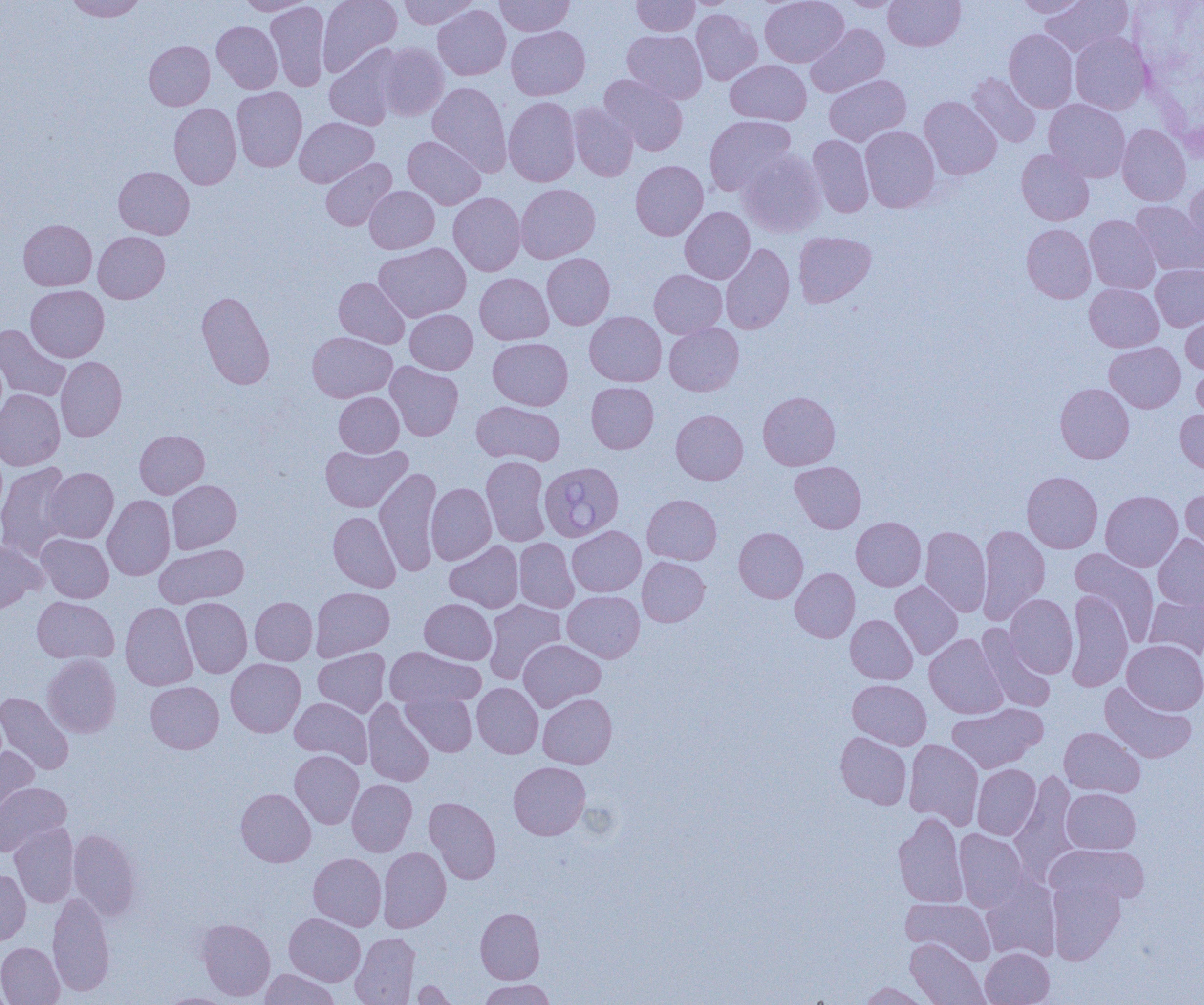
Summary:
  - Coordinate format: approximate bounding boxes as (x1,y1)-(x2,y2) corner pairs in pixels
  - Uninfected red blood cell locations: (64,0)-(147,21), (318,0)-(402,76), (399,0)-(479,29), (495,0)-(575,36), (631,0)-(699,36), (681,0)-(743,8), (760,0)-(848,67), (839,0)-(903,11), (884,0)-(965,51), (1015,0)-(1091,17), (1040,0)-(1132,57), (235,1)-(314,15), (266,2)-(330,91), (433,4)-(511,80), (691,9)-(763,84), (212,21)-(282,93), (806,24)-(889,97), (506,26)-(590,100), (1004,29)-(1078,113), (622,30)-(707,103), (1070,31)-(1151,114), (144,41)-(215,110), (378,43)-(449,121), (325,46)-(403,130), (726,60)-(811,125), (967,73)-(1041,147), (600,74)-(688,155), (824,74)-(911,145), (428,82)-(511,175), (231,87)-(307,172), (504,96)-(580,187), (920,96)-(1001,179), (1043,99)-(1130,182), (168,103)-(241,189), (568,103)-(638,181), (704,115)-(796,196), (294,117)-(378,187), (1117,123)-(1191,206), (860,126)-(940,212), (808,134)-(874,217), (403,135)-(486,209), (738,149)-(826,237), (1016,149)-(1094,225), (321,158)-(396,231), (630,160)-(708,240), (114,166)-(194,239), (1185,181)-(1204,260), (516,183)-(600,263), (364,186)-(439,253), (449,192)-(526,276), (1131,201)-(1204,276), (680,206)-(755,283), (1085,215)-(1160,294), (18,219)-(96,290), (1022,224)-(1096,303), (93,231)-(170,303), (794,232)-(876,307), (374,242)-(471,322), (720,243)-(794,334), (542,253)-(615,329), (1151,264)-(1204,331), (649,269)-(727,338), (475,273)-(553,345), (334,277)-(410,348), (1084,283)-(1163,352), (26,285)-(109,361), (196,290)-(276,389), (405,309)-(478,374), (1181,310)-(1204,374), (585,311)-(666,386), (664,322)-(743,396), (0,324)-(71,402), (307,332)-(397,402), (488,337)-(572,410), (1104,342)-(1185,413), (56,356)-(127,441), (1191,360)-(1204,424), (385,361)-(463,441), (586,382)-(659,453), (1055,383)-(1134,464), (0,389)-(65,470), (758,391)-(840,470), (334,392)-(404,457), (471,401)-(565,465), (1175,409)-(1204,474), (671,410)-(748,484), (135,430)-(209,498), (320,444)-(411,512), (481,456)-(551,546), (790,461)-(866,533), (0,462)-(74,561), (43,467)-(118,543), (375,468)-(441,576), (1022,471)-(1102,553), (167,480)-(241,553), (426,483)-(496,564), (1180,487)-(1204,564), (1100,490)-(1182,572), (642,494)-(722,564), (102,495)-(175,580), (329,511)-(401,592), (851,516)-(926,591), (976,525)-(1050,625), (567,526)-(645,596), (920,526)-(992,617), (734,527)-(808,603), (1153,533)-(1204,610), (37,534)-(113,603), (514,538)-(579,613), (0,539)-(46,614), (445,541)-(524,612), (154,544)-(249,608), (1069,548)-(1160,643), (637,557)-(710,626), (790,567)-(860,642), (889,581)-(963,659), (311,587)-(394,661), (563,590)-(644,662), (1065,590)-(1133,692), (1006,593)-(1078,677), (1144,595)-(1204,659), (32,596)-(119,664), (181,597)-(252,677), (250,597)-(317,665), (420,598)-(496,664), (483,599)-(566,683), (120,602)-(197,690), (845,615)-(917,684), (977,624)-(1055,712), (924,634)-(1008,718), (518,639)-(605,711), (1122,639)-(1204,715), (386,646)-(485,708), (314,647)-(390,717), (43,654)-(121,737), (226,658)-(306,737), (848,679)-(931,749), (146,681)-(223,753), (472,683)-(543,758), (1099,683)-(1197,763), (402,690)-(477,756), (0,692)-(73,775), (538,693)-(617,768), (290,696)-(372,766), (362,699)-(434,786), (947,703)-(1047,773), (1059,726)-(1145,798), (835,732)-(911,809), (904,739)-(984,829), (0,746)-(39,822), (290,750)-(363,828), (508,761)-(590,840), (972,764)-(1041,840), (1010,771)-(1079,883), (347,779)-(416,856), (0,783)-(70,856), (236,788)-(315,866), (1062,788)-(1140,854), (424,797)-(501,884), (893,812)-(968,908), (10,823)-(78,907), (68,829)-(141,921), (954,829)-(1029,911), (1047,844)-(1149,906), (378,847)-(451,932), (309,852)-(386,931), (0,868)-(30,945), (980,876)-(1060,962), (1046,876)-(1126,965), (48,892)-(115,996), (901,898)-(996,965), (475,907)-(544,983), (284,913)-(365,985), (197,918)-(275,1001), (350,932)-(420,1005), (906,938)-(990,1005), (0,942)-(64,1005), (981,947)-(1054,1005), (260,969)-(340,1005), (478,979)-(555,1005), (409,980)-(456,1005), (858,982)-(933,1005), (158,992)-(234,1004)
  - Babesia divergens-infected red blood cell locations: (542,465)-(626,545)
  - Slide-level diagnosis: Babesia divergens
  - Image size: 1204×1005 pixels
  - Preparation: thin blood smear
  - Field of view: single
  - Modality: light microscopy
  - Magnification: 1000x